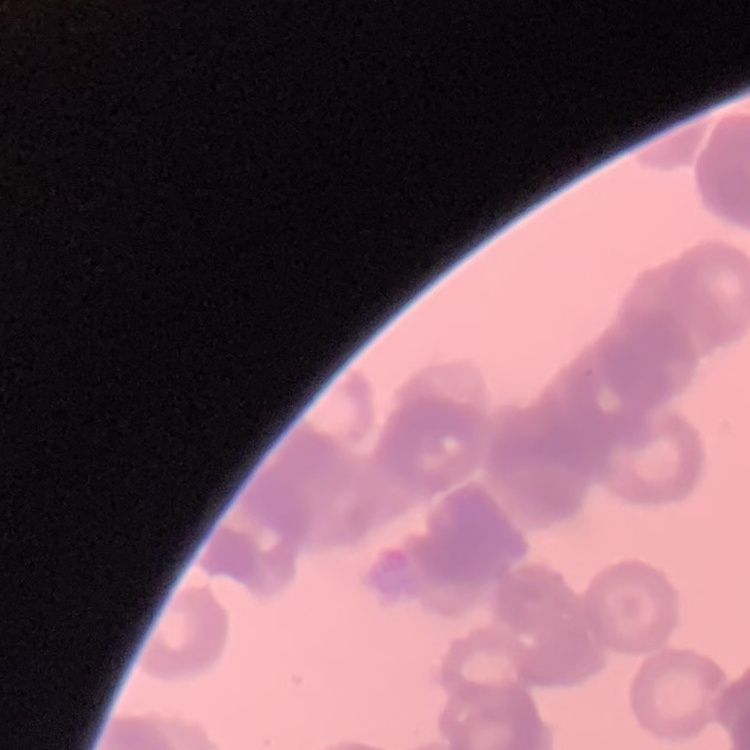

Summary:
  - Red blood cell morphology: rouleaux formation
  - Stain: Field's or Giemsa
  - Preparation: thin blood smear
  - Image type: one tile cut from a larger photomicrograph